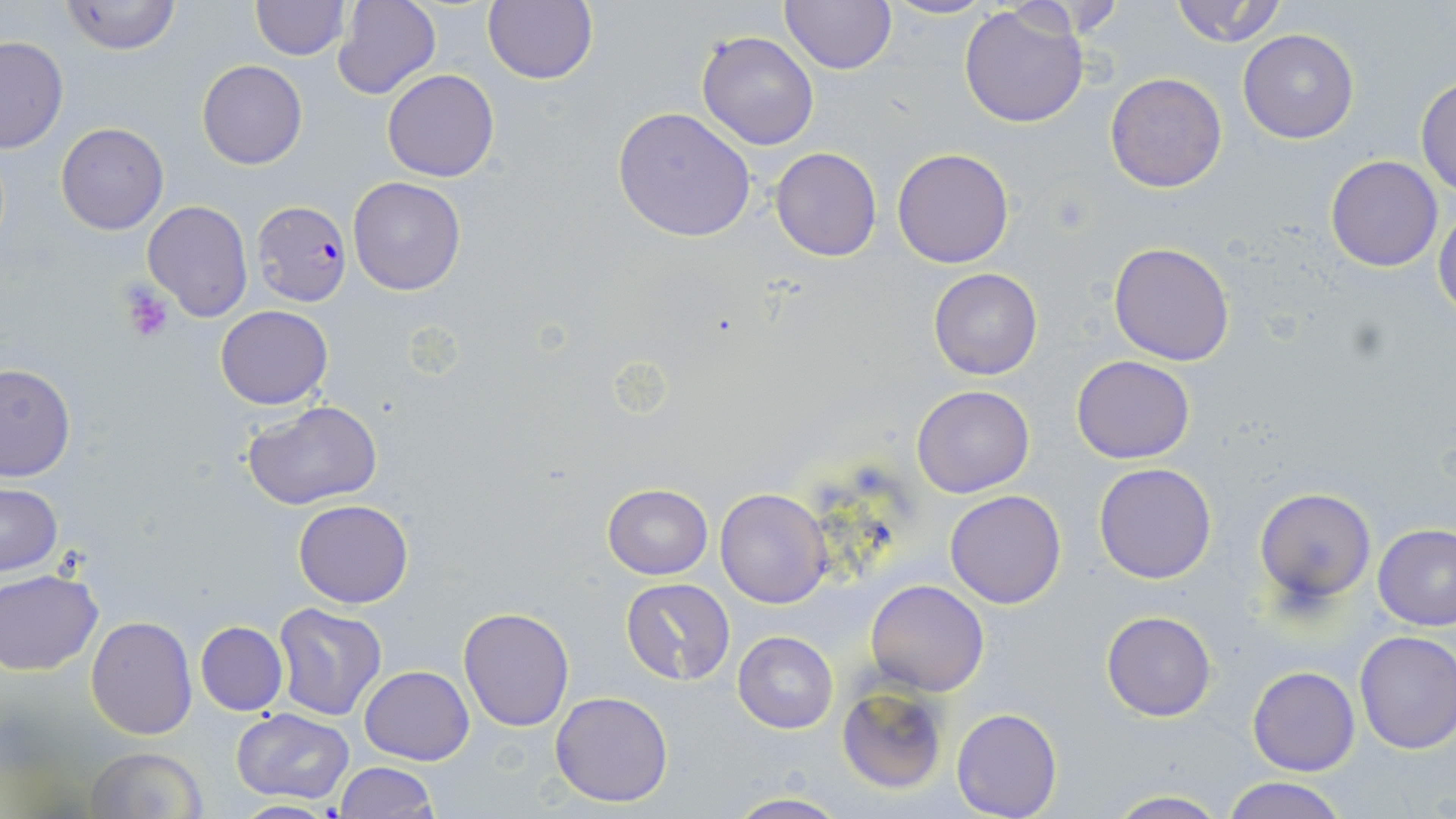
Summary:
  - Coordinate format: approximate bounding boxes as (x1, y1, x2, y2) in pixels
  - Platelet locations: (117, 283, 176, 342)
  - Uninfected red blood cell locations: (60, 0, 181, 55), (483, 0, 598, 84), (779, 0, 895, 73), (880, 0, 996, 20), (1169, 0, 1291, 48), (249, 1, 349, 60), (332, 1, 440, 100), (958, 4, 1090, 129), (1239, 29, 1359, 144), (696, 31, 819, 150), (0, 37, 69, 154), (196, 60, 306, 168), (382, 69, 499, 182), (1104, 72, 1228, 193), (1415, 76, 1456, 196), (612, 106, 756, 242), (56, 122, 168, 234), (770, 147, 882, 262), (892, 147, 1014, 267), (1325, 155, 1443, 271), (347, 175, 468, 295), (142, 201, 253, 321), (1434, 204, 1456, 322), (1109, 242, 1235, 367), (928, 268, 1042, 380), (215, 305, 332, 409), (1071, 354, 1195, 464), (0, 363, 75, 482), (912, 384, 1035, 498), (243, 400, 384, 511), (1095, 463, 1217, 584), (1, 483, 61, 576), (603, 484, 713, 580), (715, 488, 833, 608), (1254, 488, 1375, 605), (944, 490, 1067, 609), (294, 499, 412, 608), (1374, 525, 1456, 631), (0, 571, 102, 674), (621, 578, 735, 686), (865, 579, 990, 696), (273, 603, 386, 721), (458, 608, 574, 731), (1101, 611, 1216, 721), (86, 616, 197, 738), (195, 621, 288, 715), (1353, 629, 1456, 753), (733, 631, 838, 733), (359, 665, 474, 765), (1247, 665, 1360, 776), (837, 685, 948, 793), (550, 691, 675, 808), (232, 708, 355, 805), (951, 708, 1062, 819), (84, 747, 207, 819), (334, 762, 436, 819), (1223, 776, 1347, 819), (1105, 791, 1231, 819), (723, 793, 853, 819), (226, 800, 344, 817)
  - Plasmodium falciparum-infected red blood cell locations: (251, 201, 352, 305)
  - Slide-level diagnosis: Plasmodium falciparum
  - Magnification: 1000x
  - Image size: 1456×819 pixels
  - Modality: light microscopy
  - Preparation: thin blood film
  - Field of view: single
  - Stain: May-Grünwald-Giemsa